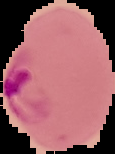
{
  "image_type": "cell region segmented out of the field of view; surrounding area masked to black",
  "result": "malaria parasites identified",
  "image_size": "115×154 pixels",
  "preparation": "thin blood film"
}